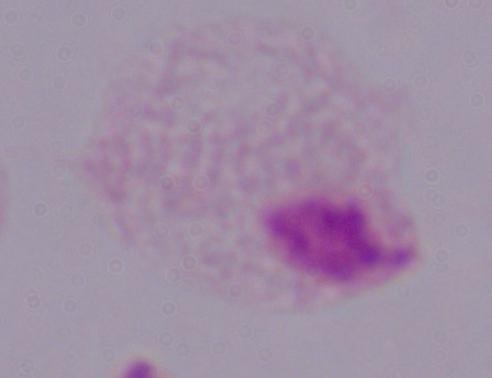
magnification: 1000x
identification: trichomonad
modality: photomicrograph